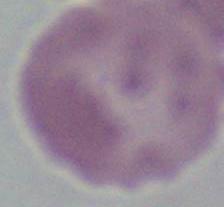

{
  "magnification": "1000x",
  "identification": "red blood cell",
  "modality": "photomicrograph"
}